Assess this cell for malaria.
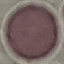
It is uninfected.

{
  "stain": "Giemsa",
  "image_type": "automatically extracted cell patch, resized to 64 × 64 pixels",
  "preparation": "thin blood film",
  "capture": "smartphone camera at the microscope eyepiece"
}